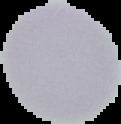

Summary:
  - Result: negative for malaria parasites
  - Image size: 121×124 pixels
  - Preparation: thin blood film
  - Image type: cell region segmented out of the field of view; surrounding area masked to black